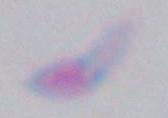

Captured at 1000x magnification. Toxoplasma gondii is seen. Photomicrograph.